Locate every parasitized RBC.
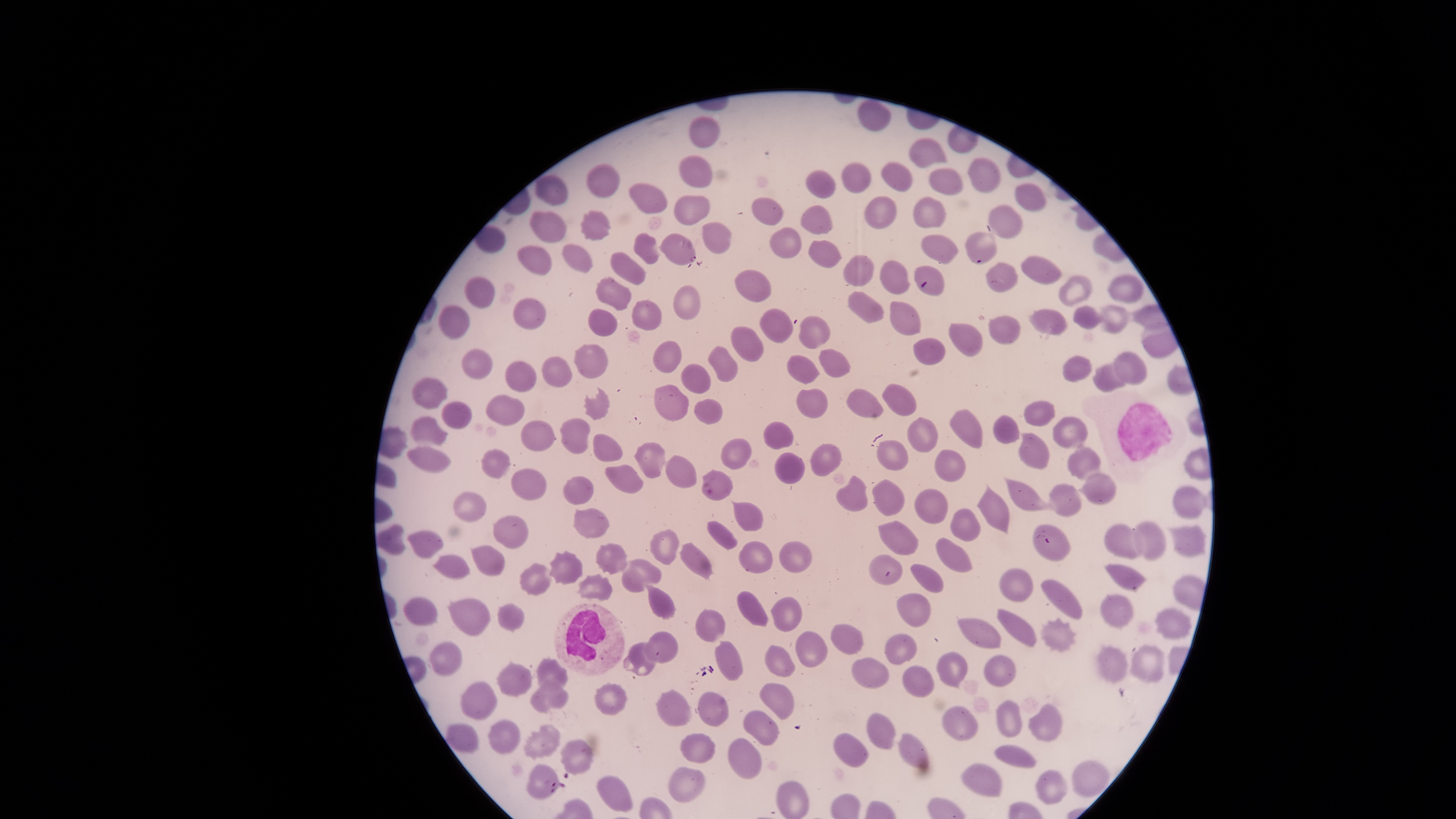
No parasitized RBCs identified.

Approximate bounding boxes as {left, top, right, bottom} in pixels.
Summary:
  - Uninfected RBCs: {690, 115, 720, 148}, {907, 139, 946, 168}, {679, 155, 713, 188}, {966, 157, 1000, 193}, {882, 160, 911, 191}, {928, 169, 963, 195}, {805, 170, 835, 198}, {535, 175, 569, 205}, {628, 183, 668, 213}, {1014, 184, 1045, 213}, {675, 195, 710, 225}, {864, 195, 897, 229}, {751, 197, 784, 226}, {913, 197, 945, 227}, {799, 204, 832, 234}, {989, 204, 1023, 238}, {580, 209, 611, 240}, {530, 211, 566, 242}, {702, 222, 731, 254}, {769, 227, 801, 258}, {966, 231, 997, 264}, {634, 233, 659, 264}, {660, 233, 695, 264}, {920, 235, 959, 264}, {808, 240, 841, 269}, {517, 245, 551, 275}, {562, 245, 592, 272}, {610, 252, 645, 287}, {842, 254, 875, 287}, {1020, 255, 1062, 285}, {879, 260, 908, 294}, {986, 262, 1017, 292}, {914, 265, 945, 296}, {735, 269, 771, 302}, {1107, 273, 1143, 303}, {1058, 274, 1092, 306}, {465, 275, 495, 310}, {596, 278, 630, 310}, {672, 285, 699, 321}, {848, 291, 884, 323}, {632, 299, 661, 330}, {889, 300, 921, 336}, {438, 305, 469, 339}, {1099, 305, 1128, 334}, {1073, 306, 1107, 330}, {760, 307, 792, 343}, {1029, 307, 1067, 335}, {587, 308, 616, 335}, {798, 315, 830, 349}, {990, 316, 1021, 344}, {948, 322, 982, 356}, {731, 326, 763, 362}, {912, 337, 947, 366}, {652, 340, 682, 372}, {708, 344, 738, 382}, {574, 345, 610, 380}, {817, 348, 850, 378}, {1112, 351, 1147, 384}, {787, 355, 819, 384}, {1062, 355, 1092, 382}, {541, 356, 572, 387}, {505, 362, 536, 392}, {1093, 362, 1130, 391}, {681, 364, 710, 393}, {411, 377, 446, 409}, {882, 382, 915, 416}, {654, 385, 689, 421}, {582, 387, 609, 420}, {796, 388, 827, 418}, {846, 389, 883, 418}, {485, 394, 525, 427}, {693, 398, 722, 425}, {442, 400, 471, 429}, {1024, 400, 1055, 427}, {948, 410, 984, 449}, {993, 415, 1019, 445}, {408, 416, 447, 445}, {1052, 417, 1089, 448}, {560, 418, 590, 454}, {907, 418, 938, 452}, {521, 420, 553, 450}, {763, 422, 794, 451}, {1019, 432, 1049, 470}, {593, 435, 623, 461}, {721, 438, 751, 469}, {877, 440, 909, 470}, {1069, 441, 1100, 479}, {634, 443, 665, 479}, {810, 443, 841, 477}, {408, 447, 451, 472}, {481, 449, 510, 477}, {934, 450, 966, 481}, {665, 453, 697, 487}, {773, 453, 805, 485}, {604, 463, 643, 494}, {511, 468, 548, 500}, {700, 468, 733, 501}, {1078, 472, 1116, 504}, {835, 475, 869, 512}, {563, 476, 592, 506}, {1004, 476, 1055, 511}, {871, 478, 905, 516}, {977, 483, 1010, 534}, {1048, 485, 1081, 517}, {1171, 485, 1204, 517}, {913, 489, 947, 524}, {453, 491, 487, 524}, {731, 501, 762, 532}, {573, 508, 609, 539}, {948, 508, 981, 541}, {493, 513, 529, 549}, {706, 521, 738, 549}, {877, 521, 920, 555}, {1132, 521, 1166, 558}, {1104, 523, 1144, 559}, {1033, 525, 1071, 562}, {1166, 526, 1206, 558}, {407, 530, 442, 558}, {650, 530, 679, 564}, {936, 537, 974, 573}, {778, 540, 812, 573}, {738, 541, 773, 573}, {596, 542, 627, 573}, {681, 543, 712, 579}, {471, 544, 506, 576}, {548, 551, 582, 584}, {868, 554, 902, 585}, {620, 559, 663, 591}, {519, 562, 555, 596}, {909, 564, 944, 593}, {1103, 564, 1145, 591}, {999, 568, 1032, 602}, {576, 573, 612, 600}, {1040, 578, 1082, 620}, {643, 584, 674, 618}, {736, 591, 768, 627}, {896, 591, 930, 627}, {1100, 593, 1134, 628}, {404, 596, 438, 625}, {447, 596, 491, 636}, {770, 596, 803, 632}, {497, 602, 524, 631}, {695, 609, 726, 641}, {997, 609, 1035, 647}, {1155, 609, 1191, 640}, {956, 617, 1001, 648}, {1040, 617, 1076, 652}, {830, 623, 863, 654}, {643, 632, 678, 664}, {796, 632, 828, 667}, {884, 634, 918, 664}, {428, 641, 462, 675}, {623, 641, 658, 677}, {715, 641, 742, 681}, {765, 645, 796, 677}, {1096, 645, 1127, 682}, {1132, 645, 1164, 683}, {937, 652, 967, 690}, {984, 655, 1017, 686}, {851, 656, 889, 690}, {536, 659, 567, 689}, {497, 662, 531, 695}, {902, 666, 934, 697}, {530, 677, 567, 713}, {461, 681, 497, 720}, {594, 683, 626, 715}, {760, 684, 794, 719}, {655, 690, 691, 726}, {697, 692, 728, 727}, {996, 699, 1022, 737}, {1028, 703, 1062, 742}, {942, 706, 979, 742}, {743, 709, 779, 745}, {867, 713, 894, 750}, {488, 720, 520, 754}, {445, 723, 479, 754}, {522, 724, 560, 756}, {680, 733, 716, 763}, {833, 733, 869, 767}, {898, 733, 928, 768}, {559, 738, 594, 774}, {728, 738, 761, 779}, {994, 745, 1035, 767}, {1070, 759, 1110, 797}, {961, 763, 1002, 797}, {527, 764, 558, 797}, {667, 767, 705, 801}, {1036, 770, 1067, 804}, {596, 776, 632, 812}, {775, 781, 808, 819}
  - WBCs: {1082, 387, 1187, 485}, {554, 603, 624, 676}
  - Stain: Giemsa
  - Image size: 1456×819 pixels
  - Capture: smartphone photograph through the microscope eyepiece
  - Preparation: thin blood smear
  - Field of view: single
  - Visible region: circular